Identify the blood parasite species.
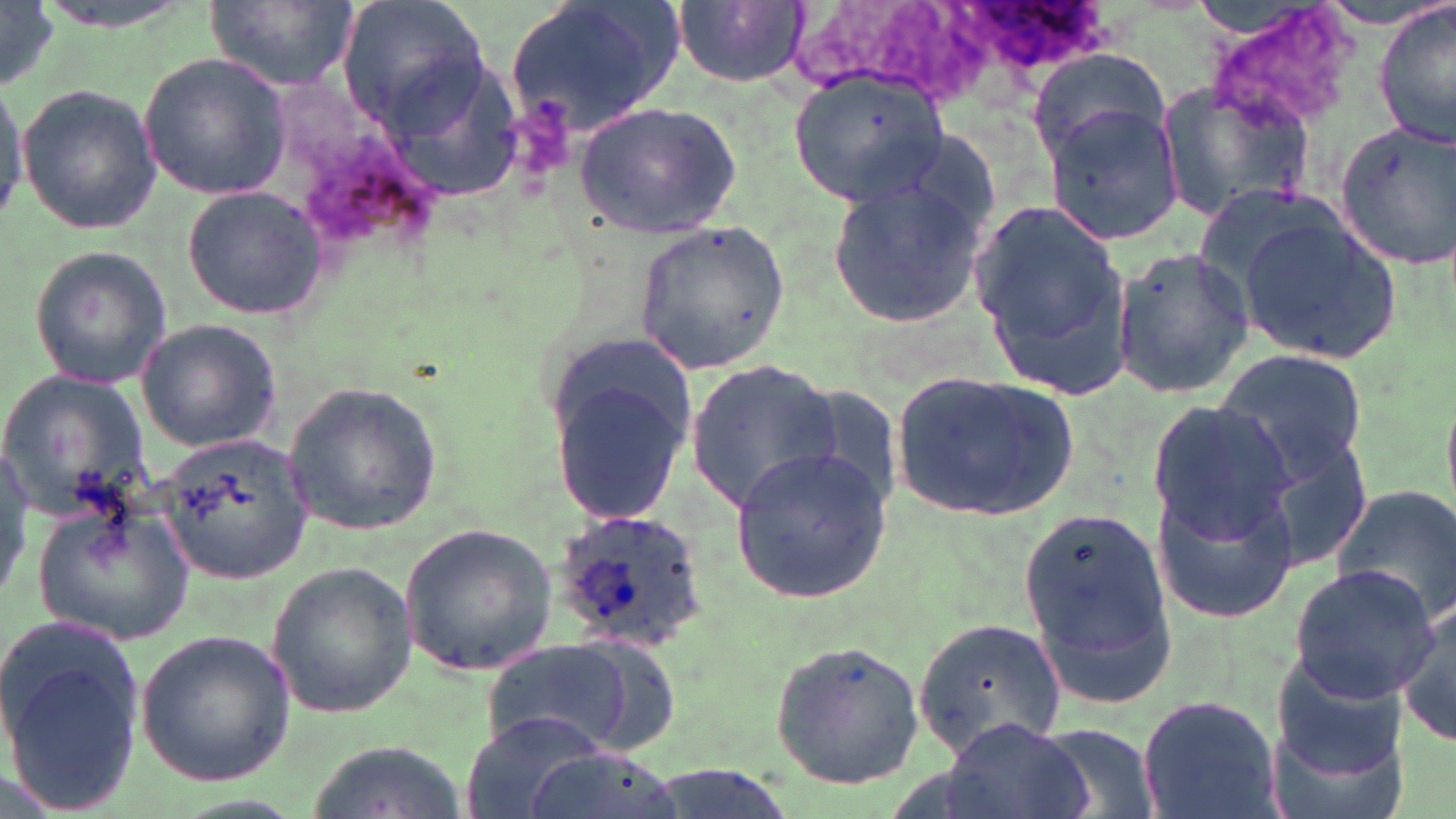
Plasmodium ovale.

field of view = single
magnification = 1000x
preparation = thin blood film
image size = 1456×819 pixels
Plasmodium ovale-infected red blood cell locations = approximate bounding boxes as (x1,y1)-(x2,y2) corner pairs in pixels: (547,509)-(706,652)
modality = light microscopy
uninfected red blood cell locations = approximate bounding boxes as (x1,y1)-(x2,y2) corner pairs in pixels: (209,0)-(355,91), (339,0)-(489,136), (504,0)-(681,139), (673,2)-(810,87), (1374,2)-(1455,147), (1,3)-(56,92), (1200,4)-(1362,137), (1027,48)-(1174,160), (137,54)-(292,201), (790,69)-(949,209), (1155,79)-(1315,223), (0,81)-(30,231), (17,82)-(161,234), (577,100)-(741,238), (1041,100)-(1186,247), (1336,120)-(1456,268), (825,172)-(987,331), (182,186)-(329,320), (970,196)-(1136,400), (1235,212)-(1404,363), (633,222)-(790,374), (27,243)-(174,392), (1114,246)-(1253,401), (134,315)-(283,454), (542,338)-(700,528), (1213,346)-(1372,485), (683,359)-(842,513), (890,367)-(1081,523), (0,368)-(155,527), (281,379)-(444,538), (794,384)-(908,512), (1146,398)-(1298,547), (157,430)-(316,583), (0,441)-(34,604), (731,448)-(895,603), (1153,469)-(1303,625), (1329,485)-(1456,625), (32,494)-(198,651), (1020,502)-(1179,714), (400,521)-(558,679), (264,559)-(418,717), (1290,563)-(1437,699), (1395,601)-(1456,747), (912,614)-(1068,762), (1,616)-(147,817), (134,628)-(298,787), (484,639)-(635,757), (769,639)-(929,791), (1270,644)-(1408,793), (1134,693)-(1282,819), (461,711)-(609,819), (944,719)-(1090,819), (1033,722)-(1161,819), (302,740)-(466,819), (525,747)-(683,819)
stain = May-Grünwald-Giemsa